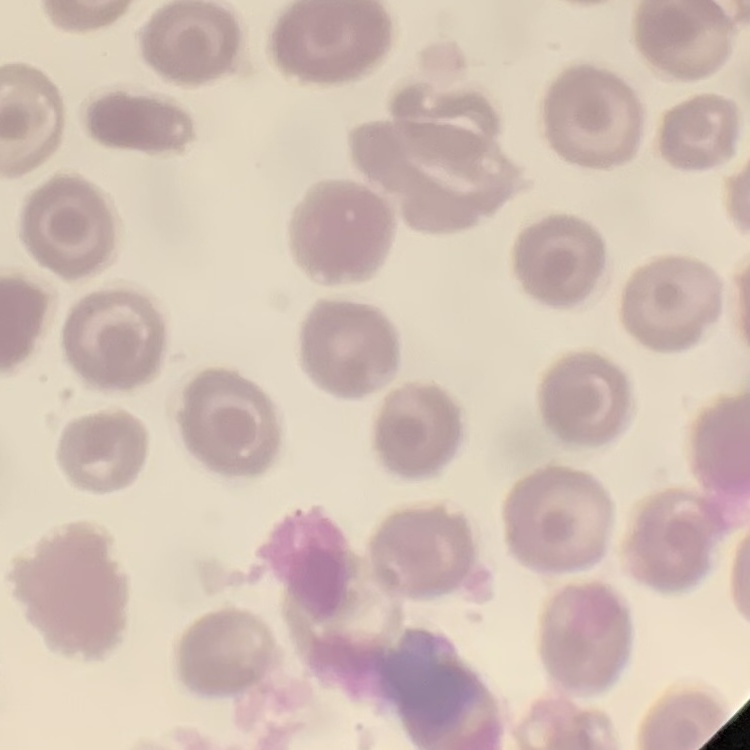

Summary:
  - Erythrocyte morphology: no rouleaux formation
  - Image type: one tile cut from a larger photomicrograph
  - Preparation: thin blood smear
  - Stain: Field's or Giemsa